Draw a bounding box around every parasitised red blood cell.
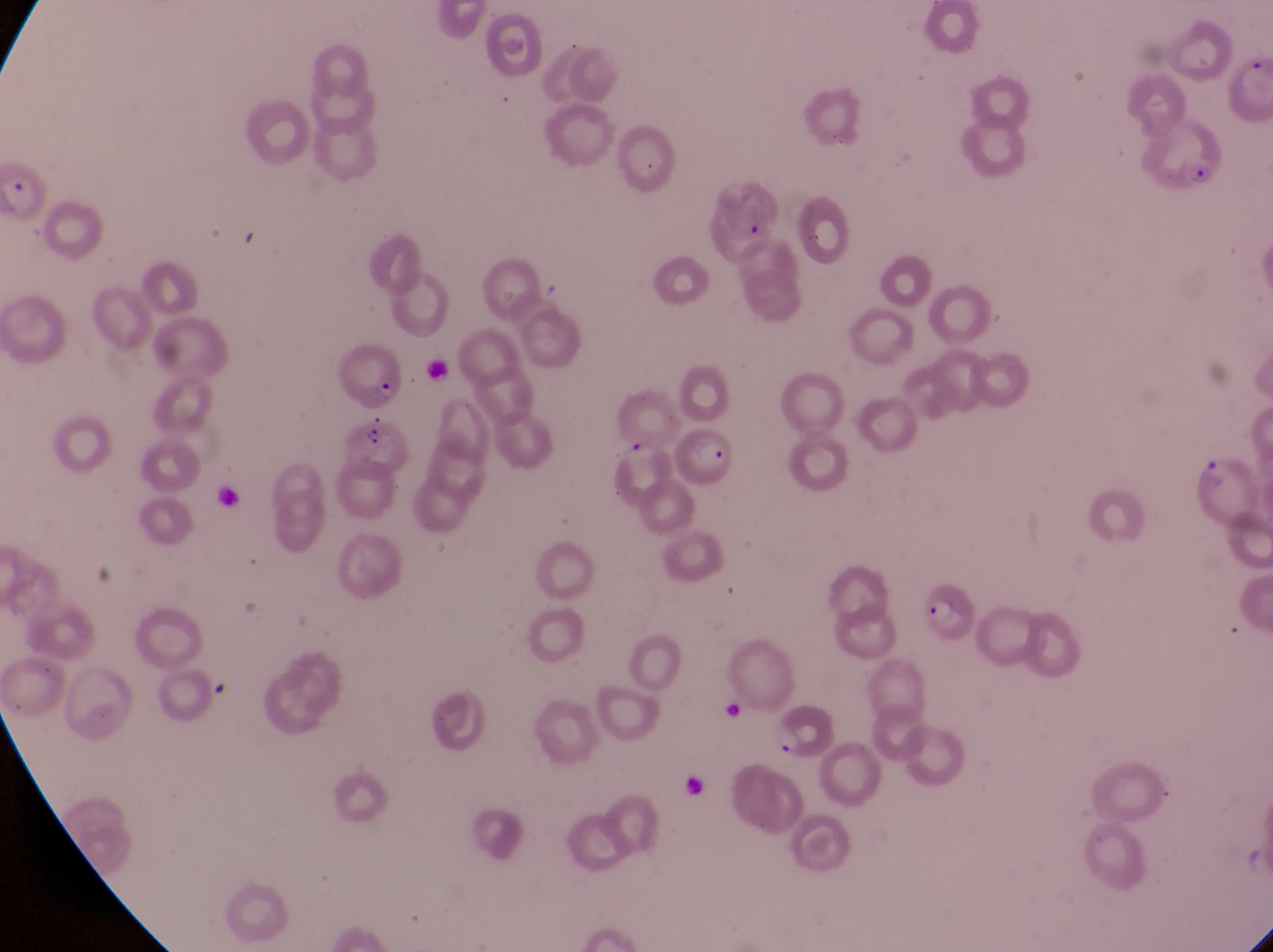

Approximate bounding boxes as {left, top, right, bottom} in pixels.
Parasitised red blood cells: {1142, 120, 1235, 199}, {704, 180, 779, 252}, {339, 344, 402, 404}, {679, 420, 744, 490}, {1195, 449, 1253, 517}, {917, 575, 980, 645}.

Trophozoite locations: {771, 719, 803, 759}. Artifact (platelet-like body, stain precipitate, or debris) locations: {3, 169, 51, 214}, {364, 425, 399, 455}, {607, 435, 655, 465}. One field of view. Image is 1273×952 pixels. Sample from Uganda. Photographed through the eyepiece of an Olympus CX-23 microscope with a smartphone camera. Magnification of 1000x. Thin blood smear.